Outline each blood parasite and name the species.
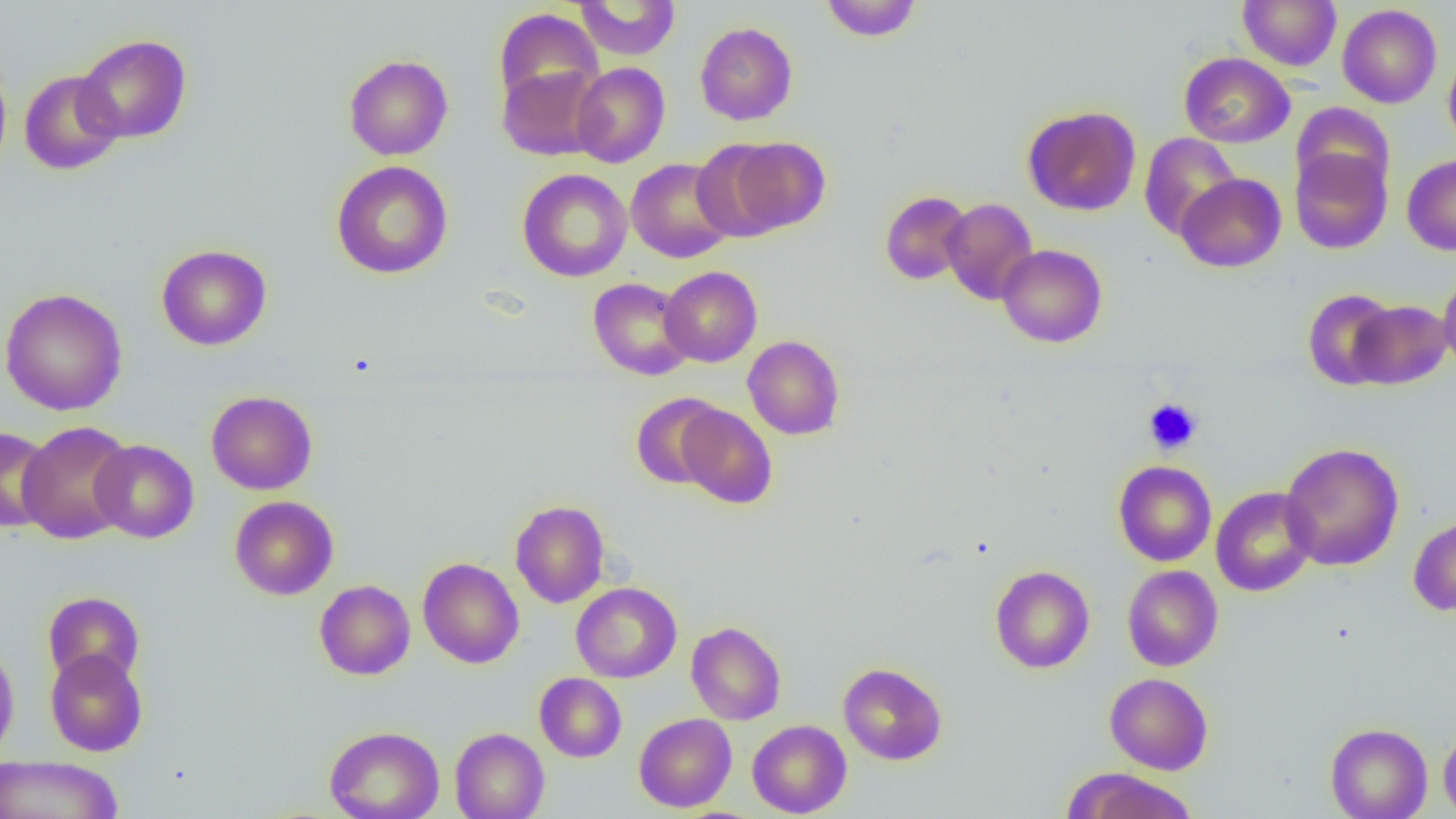

No blood parasites seen.

Approximate bounding boxes as named x1/y1/x2/y2 corners in pixels. Platelet locations: (x1=1143, y1=398, x2=1203, y2=455). Uninfected red blood cell locations: (x1=819, y1=0, x2=923, y2=42), (x1=1237, y1=0, x2=1342, y2=70), (x1=574, y1=1, x2=681, y2=60), (x1=1337, y1=4, x2=1442, y2=108), (x1=493, y1=9, x2=604, y2=109), (x1=694, y1=21, x2=798, y2=126), (x1=75, y1=34, x2=192, y2=144), (x1=1443, y1=51, x2=1456, y2=152), (x1=1178, y1=52, x2=1295, y2=148), (x1=343, y1=54, x2=454, y2=160), (x1=0, y1=57, x2=12, y2=180), (x1=570, y1=62, x2=670, y2=168), (x1=497, y1=65, x2=605, y2=161), (x1=19, y1=70, x2=124, y2=175), (x1=1291, y1=102, x2=1394, y2=198), (x1=1022, y1=105, x2=1141, y2=216), (x1=1139, y1=133, x2=1241, y2=240), (x1=715, y1=136, x2=830, y2=238), (x1=1289, y1=145, x2=1392, y2=254), (x1=1402, y1=155, x2=1456, y2=255), (x1=625, y1=157, x2=735, y2=263), (x1=331, y1=160, x2=453, y2=279), (x1=517, y1=168, x2=632, y2=282), (x1=1175, y1=173, x2=1286, y2=272), (x1=880, y1=190, x2=974, y2=285), (x1=942, y1=197, x2=1038, y2=305), (x1=156, y1=244, x2=272, y2=350), (x1=997, y1=244, x2=1107, y2=347), (x1=660, y1=266, x2=762, y2=367), (x1=1438, y1=272, x2=1456, y2=374), (x1=588, y1=278, x2=696, y2=380), (x1=0, y1=288, x2=127, y2=415), (x1=1302, y1=288, x2=1400, y2=389), (x1=1348, y1=300, x2=1452, y2=389), (x1=743, y1=335, x2=845, y2=440), (x1=206, y1=391, x2=318, y2=495), (x1=630, y1=393, x2=727, y2=489), (x1=676, y1=404, x2=777, y2=509), (x1=17, y1=421, x2=135, y2=544), (x1=0, y1=425, x2=55, y2=533), (x1=90, y1=439, x2=199, y2=543), (x1=1279, y1=442, x2=1404, y2=571), (x1=1114, y1=460, x2=1216, y2=566), (x1=1210, y1=487, x2=1319, y2=596), (x1=230, y1=496, x2=339, y2=600), (x1=510, y1=500, x2=610, y2=608), (x1=1408, y1=514, x2=1456, y2=616), (x1=418, y1=558, x2=524, y2=668), (x1=990, y1=565, x2=1095, y2=673), (x1=1122, y1=565, x2=1223, y2=671), (x1=314, y1=580, x2=416, y2=680), (x1=571, y1=582, x2=682, y2=683), (x1=42, y1=591, x2=145, y2=688), (x1=686, y1=621, x2=786, y2=725), (x1=0, y1=638, x2=20, y2=765), (x1=45, y1=648, x2=148, y2=756), (x1=838, y1=662, x2=947, y2=765), (x1=534, y1=673, x2=627, y2=762), (x1=1104, y1=673, x2=1213, y2=774), (x1=634, y1=713, x2=737, y2=812), (x1=747, y1=719, x2=851, y2=817), (x1=1325, y1=723, x2=1432, y2=819), (x1=1438, y1=723, x2=1456, y2=818), (x1=325, y1=725, x2=445, y2=819), (x1=450, y1=727, x2=549, y2=819), (x1=0, y1=754, x2=123, y2=819), (x1=1067, y1=768, x2=1198, y2=818). Slide-level diagnosis: no evidence of blood parasites. Optical microscopy. Captured at 1000x magnification. Image is 1456×819 pixels. Thin blood film. One field of a larger specimen.